Give the extent of all uninfected red blood cells.
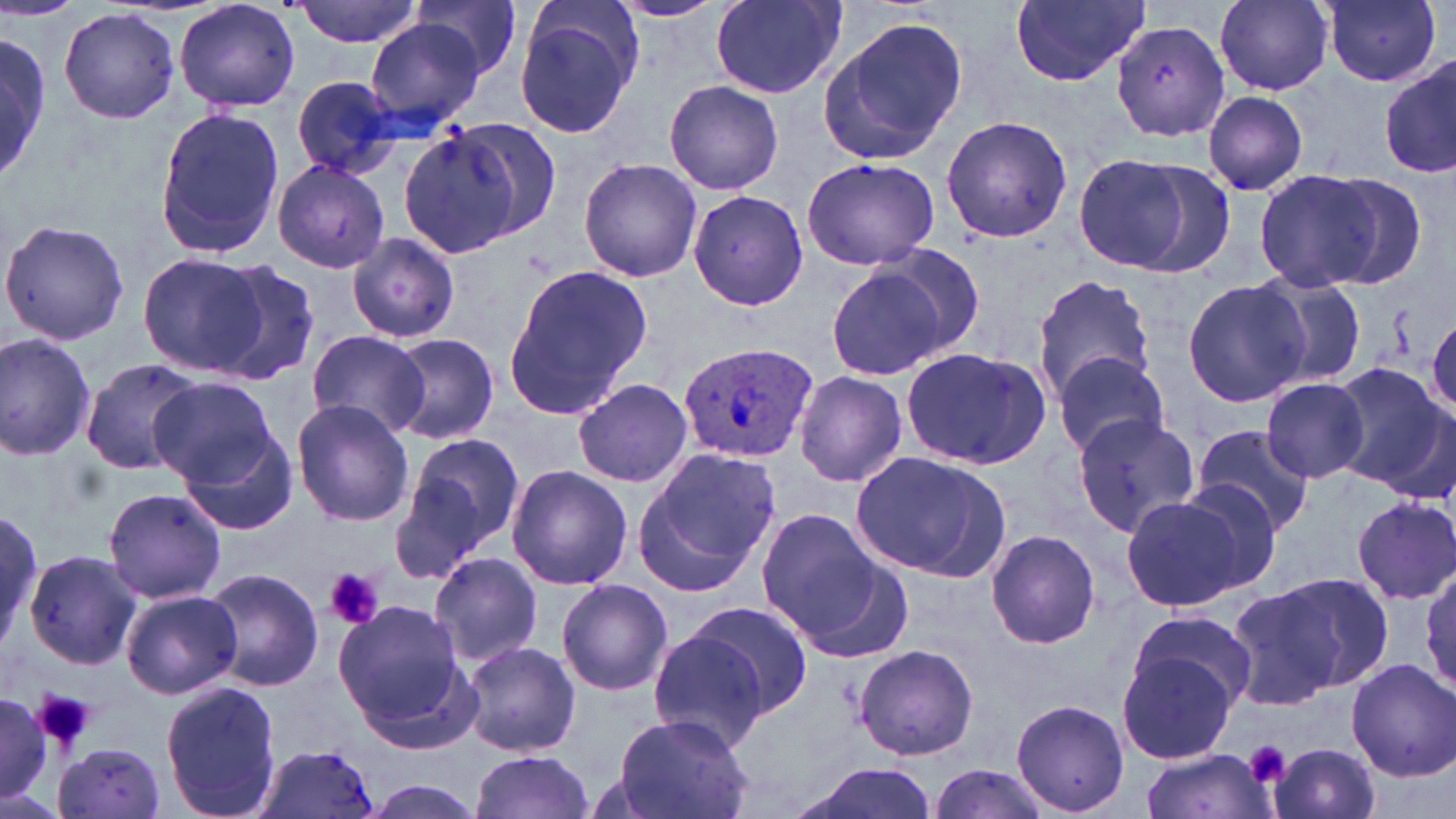

Approximate bounding boxes as (x1,y1)-(x2,y2) corner pairs in pixels.
Uninfected red blood cells: (0,0)-(81,22), (290,0)-(424,49), (1009,0)-(1149,87), (1213,0)-(1336,94), (1320,0)-(1443,87), (175,1)-(300,114), (411,1)-(522,82), (607,1)-(728,22), (710,2)-(844,98), (514,3)-(642,138), (59,9)-(180,125), (818,17)-(965,167), (366,19)-(488,128), (1111,19)-(1230,141), (0,35)-(53,183), (1380,59)-(1456,179), (291,75)-(405,181), (661,79)-(786,194), (1202,90)-(1309,197), (153,109)-(287,259), (940,114)-(1073,245), (447,117)-(562,240), (398,127)-(522,258), (1074,154)-(1216,277), (802,156)-(939,270), (578,157)-(702,282), (272,159)-(390,274), (1253,170)-(1388,292), (1312,172)-(1429,288), (688,188)-(808,314), (0,217)-(130,348), (347,232)-(460,346), (137,252)-(268,377), (825,258)-(966,381), (203,262)-(321,387), (500,264)-(653,424), (1251,271)-(1370,389), (1030,274)-(1158,401), (1182,277)-(1311,408), (304,330)-(431,439), (0,332)-(98,462), (384,332)-(499,444), (898,345)-(1050,470), (1053,356)-(1173,457), (79,357)-(204,475), (1328,363)-(1449,488), (792,371)-(908,488), (148,377)-(275,485), (1261,378)-(1371,485), (573,379)-(693,488), (293,399)-(412,527), (1068,407)-(1196,541), (1189,425)-(1316,535), (182,430)-(297,536), (394,431)-(524,575), (632,448)-(781,592), (849,450)-(1008,581), (506,463)-(632,590), (1174,478)-(1285,593), (102,486)-(227,605), (1119,494)-(1251,612), (1352,497)-(1456,603), (0,498)-(44,653), (753,510)-(894,654), (986,530)-(1100,649), (25,549)-(146,672), (425,550)-(545,669), (1420,561)-(1456,694), (202,567)-(324,692), (1234,572)-(1388,703), (555,579)-(673,697), (121,588)-(241,700), (687,600)-(813,721), (332,602)-(472,741), (1129,610)-(1257,718), (645,630)-(771,752), (1116,640)-(1244,765), (461,642)-(582,757), (852,642)-(979,760), (1346,659)-(1455,780), (160,681)-(282,819), (0,692)-(52,801), (1010,700)-(1130,816), (610,713)-(755,819), (53,741)-(167,819), (1267,742)-(1382,819), (253,744)-(380,818), (1138,749)-(1276,819), (468,752)-(594,819), (792,760)-(942,819), (927,761)-(1058,818), (360,776)-(490,818).

Platelet locations: (325,568)-(385,631), (32,689)-(96,750), (1243,740)-(1291,786). Plasmodium ovale-infected red blood cell locations: (679,343)-(815,464). Slide-level diagnosis: Plasmodium ovale. Light microscopy. One field of a larger specimen. Captured at 1000x magnification. May-Grünwald-Giemsa-stained preparation. Thin blood smear. Image is 1456×819 pixels.